Report the malaria status of this cell.
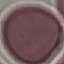
It is uninfected.

Giemsa-stained preparation. Automatically extracted cell patch, resized to 64 × 64 pixels. Acquired by smartphone through the microscope eyepiece. Thin blood film.